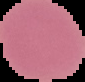
image type = segmented cell region with the area outside set to black
preparation = thin blood smear
image size = 85×82 pixels
malaria status = uninfected